Report the malaria status of this cell.
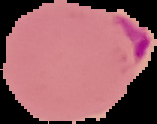
Parasitized.

Summary:
  - Preparation: thin blood smear
  - Image type: segmented cell region with the area outside set to black
  - Image size: 157×124 pixels